Identify the cell.
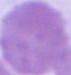

An erythrocyte.

Captured at 1000x magnification. Micrograph.